Find each white blood cell.
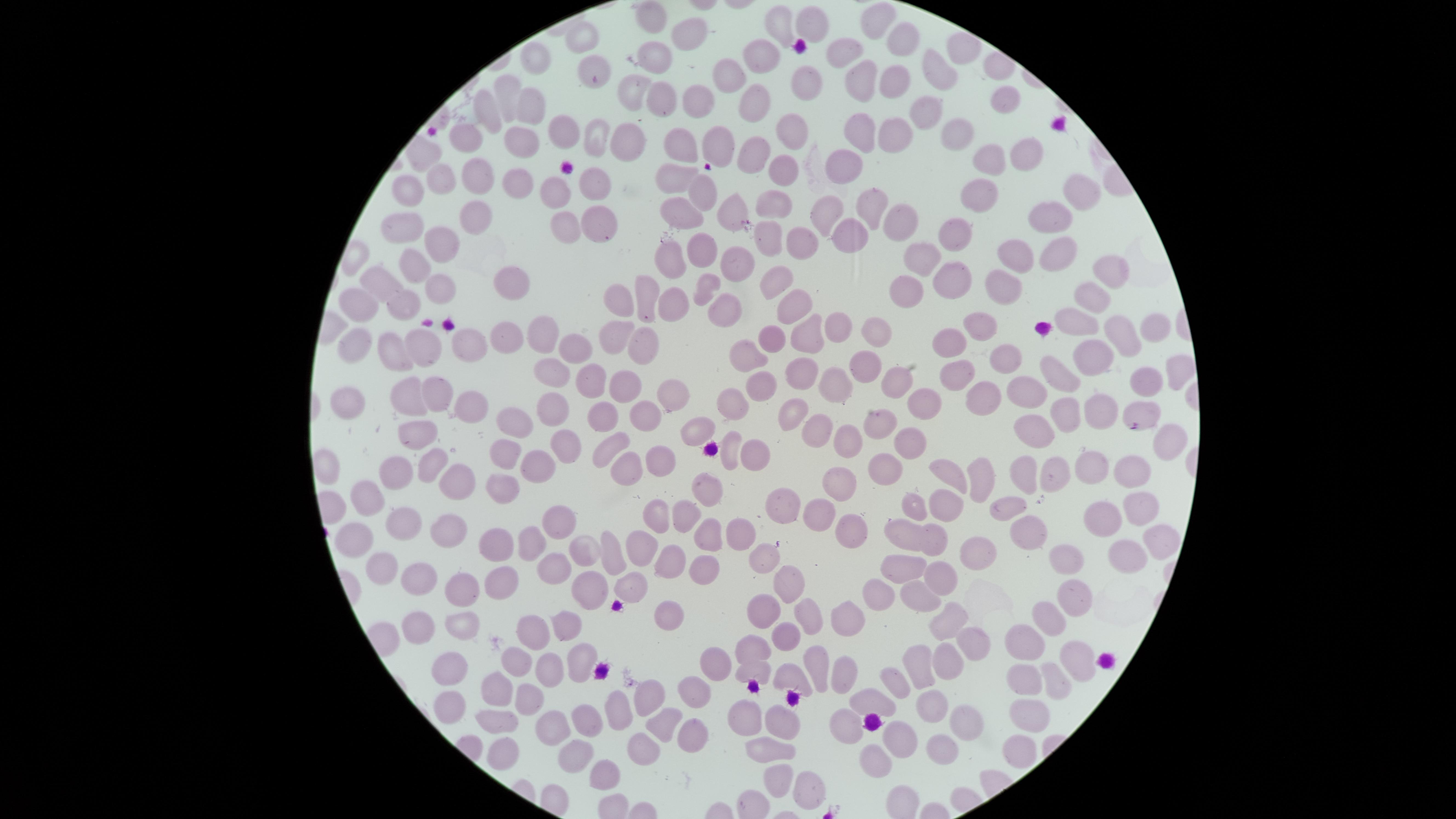
No white blood cells identified.

Approximate marker points as (x, y) in pixels. Uninfected red blood cells: (650, 15), (872, 16), (780, 21), (812, 21), (687, 35), (904, 38), (583, 44), (840, 52), (960, 53), (654, 54), (762, 54), (531, 55), (591, 68), (936, 69), (726, 77), (801, 78), (892, 82), (858, 84), (507, 87), (632, 90), (660, 96), (695, 100), (1001, 102), (753, 103), (528, 106), (927, 108), (487, 113), (792, 128), (564, 129), (895, 131), (859, 132), (952, 134), (468, 137), (627, 137), (518, 138), (597, 139), (720, 140), (678, 143), (1025, 152), (751, 153), (988, 159), (784, 167), (845, 169), (479, 175), (676, 177), (519, 178), (437, 180), (596, 182), (704, 194), (1077, 194), (405, 195), (554, 195), (978, 195), (776, 202), (870, 203), (678, 210), (1053, 212), (732, 214), (827, 214), (472, 217), (893, 218), (602, 221), (409, 222), (854, 228), (566, 231), (956, 232), (769, 234), (444, 240), (802, 243), (706, 252), (1051, 253), (923, 254), (1013, 256), (669, 259), (737, 260), (414, 263), (1111, 273), (502, 278), (951, 279), (384, 282), (776, 282), (706, 284), (907, 285), (441, 288), (1002, 288), (1093, 298), (407, 302), (643, 302), (676, 304), (361, 305), (615, 306), (791, 307), (722, 311), (1079, 319), (837, 327), (983, 328), (1151, 329), (539, 332), (505, 333), (877, 333), (1115, 334), (810, 335), (606, 337), (769, 337), (466, 342), (949, 342), (634, 343), (355, 344), (421, 347), (576, 351), (387, 353), (745, 353), (1091, 357), (1001, 358), (862, 366), (1173, 370), (549, 371), (1058, 371), (797, 372), (959, 374), (590, 379), (897, 381), (1146, 382), (623, 383), (756, 386), (835, 386), (1029, 389), (398, 391), (436, 391), (665, 394), (981, 395), (929, 399), (341, 402), (730, 402), (466, 403), (1102, 405), (1141, 407), (554, 409), (639, 410), (794, 410), (599, 412), (1064, 416), (879, 417), (512, 418), (694, 425), (1035, 427), (416, 432), (853, 442), (1169, 442), (905, 444), (561, 445), (611, 445), (506, 453), (726, 453), (745, 453), (538, 461), (659, 463), (881, 464), (431, 465), (632, 466), (1051, 469), (1092, 469), (1027, 470), (984, 471), (1131, 471), (395, 473), (949, 475), (456, 480), (838, 481), (499, 482), (706, 489), (367, 496), (910, 502), (781, 505), (941, 506), (1010, 507), (1134, 510), (658, 517), (683, 519), (821, 519), (399, 522), (561, 522), (1102, 522), (443, 528), (738, 529), (850, 531), (1026, 533), (931, 535), (707, 538), (902, 538), (358, 540), (527, 544), (1153, 544), (492, 546), (579, 546), (610, 548), (643, 548), (765, 549), (971, 550), (1124, 557), (1064, 559), (671, 562), (384, 569), (553, 569), (698, 570), (900, 570), (415, 572), (941, 575), (498, 579), (786, 584), (631, 586), (588, 590), (460, 594), (915, 595), (877, 597), (1072, 601), (761, 611), (668, 613), (1046, 617), (945, 619), (418, 621), (458, 622), (808, 622), (842, 622), (566, 626), (532, 635), (784, 639), (1029, 643), (967, 647), (749, 652), (576, 659), (1075, 659), (947, 661), (718, 663), (816, 665), (517, 666), (919, 666), (752, 668), (450, 669), (547, 670), (841, 671), (1021, 675), (789, 676), (895, 679), (1052, 682), (496, 688), (692, 693), (643, 699), (530, 701), (870, 703), (929, 705), (617, 710), (450, 711), (1028, 715), (745, 717), (961, 719), (844, 720), (549, 721), (496, 722), (581, 723), (657, 726), (776, 726), (684, 730), (899, 741), (942, 742), (638, 745), (765, 746), (1014, 749), (501, 751), (573, 755), (875, 764), (607, 775), (777, 778), (810, 787). Giemsa stain. Presence: no malaria parasites identified. Single field of view. Circular visible region. Smartphone photograph through the microscope eyepiece. Thin smear of blood. Image is 1456×819 pixels.